State which cell type is depicted.
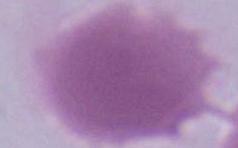
An erythrocyte.

Summary:
  - Magnification: 1000x
  - Modality: photomicrograph